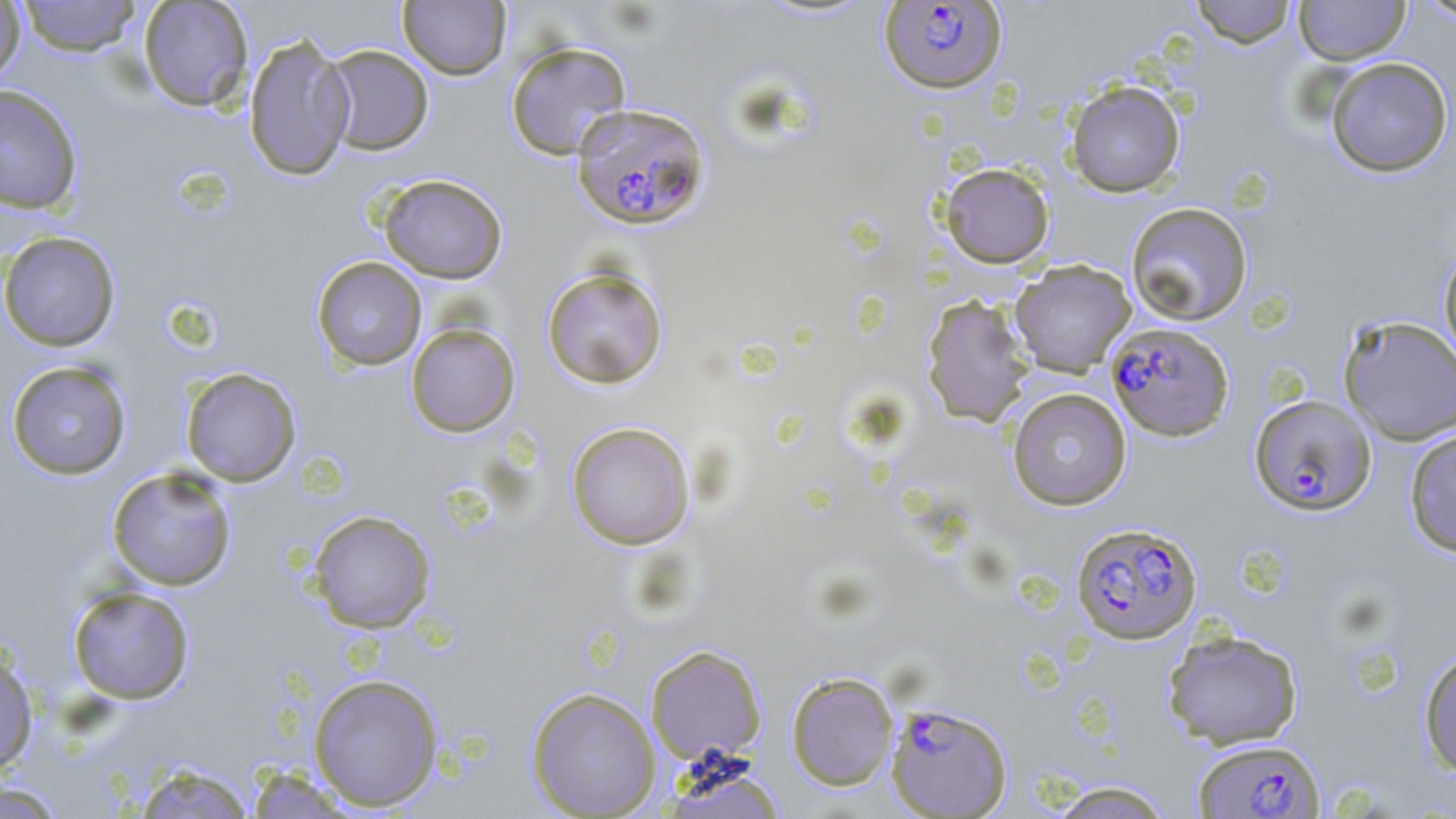 Approximate bounding boxes as [x1, y1, x2, y2] in pixels. Plasmodium falciparum-infected red blood cell locations: [879, 1, 1007, 95], [571, 102, 710, 231], [1106, 322, 1234, 441], [1249, 394, 1376, 515], [1070, 522, 1202, 645], [885, 701, 1012, 818], [1192, 737, 1325, 818]. Uninfected red blood cell locations: [16, 0, 143, 57], [137, 0, 254, 111], [1190, 0, 1297, 48], [1293, 0, 1411, 65], [1413, 0, 1456, 24], [0, 1, 26, 85], [398, 1, 511, 80], [242, 31, 356, 181], [505, 41, 632, 160], [321, 44, 434, 155], [1325, 57, 1453, 177], [1064, 80, 1186, 197], [0, 84, 84, 215], [940, 162, 1054, 268], [378, 174, 508, 284], [1125, 202, 1253, 326], [0, 231, 121, 351], [1438, 243, 1456, 371], [311, 256, 427, 371], [1010, 260, 1136, 377], [541, 267, 668, 389], [922, 294, 1035, 427], [1338, 314, 1456, 445], [406, 323, 520, 437], [6, 360, 132, 479], [180, 368, 301, 487], [1007, 387, 1132, 511], [566, 421, 695, 550], [1404, 427, 1456, 557], [106, 467, 237, 591], [308, 510, 436, 633], [67, 586, 195, 705], [1162, 628, 1304, 749], [645, 644, 767, 764], [0, 646, 38, 775], [1418, 650, 1456, 776], [786, 671, 899, 790], [309, 673, 444, 811], [526, 687, 661, 818], [128, 762, 258, 819], [243, 766, 361, 818], [665, 766, 787, 819], [1045, 779, 1177, 819], [0, 780, 69, 818]. Slide-level diagnosis: Plasmodium falciparum. Thin blood film. One field of a larger specimen. Image is 1456×819 pixels. Captured at 1000x magnification. May-Grünwald-Giemsa stain. Optical microscopy.